Comment on the morphology of the red blood cells.
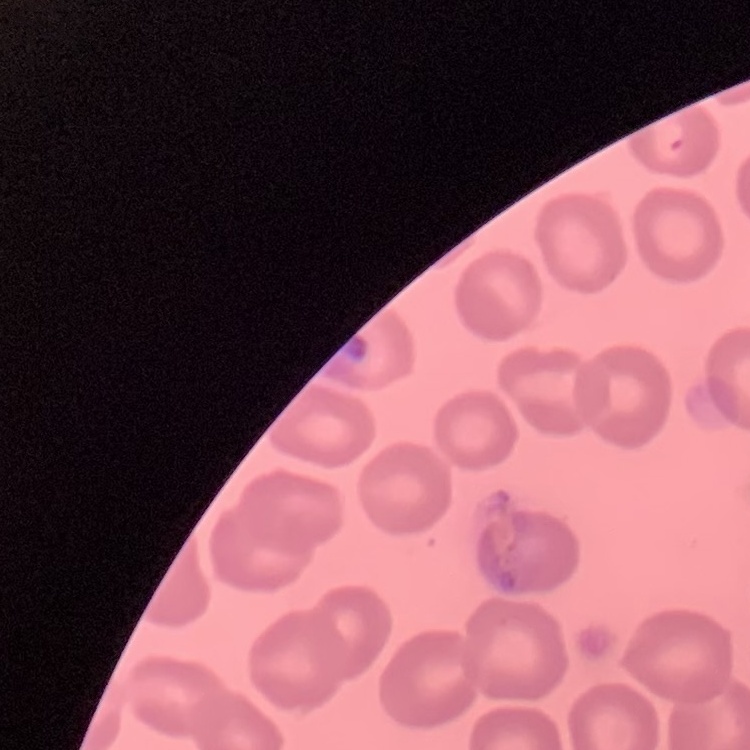

No rouleaux formation.

Stained with either Field's or Giemsa. Thin blood smear. One tile cut from a larger photomicrograph.